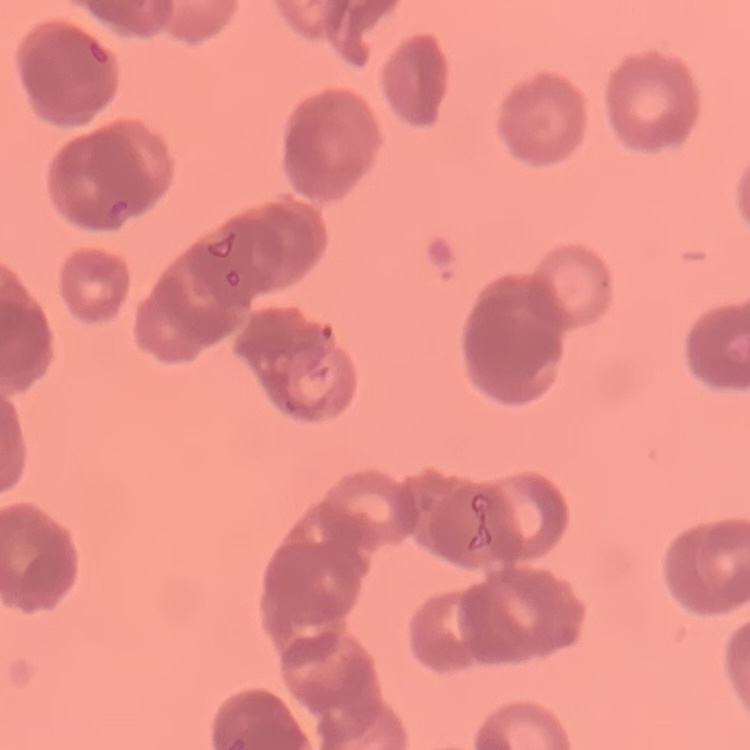

{
  "erythrocyte_morphology": "rouleaux formation",
  "stain": "Field's or Giemsa",
  "image_type": "one tile cut from a larger photomicrograph",
  "preparation": "thin blood smear"
}